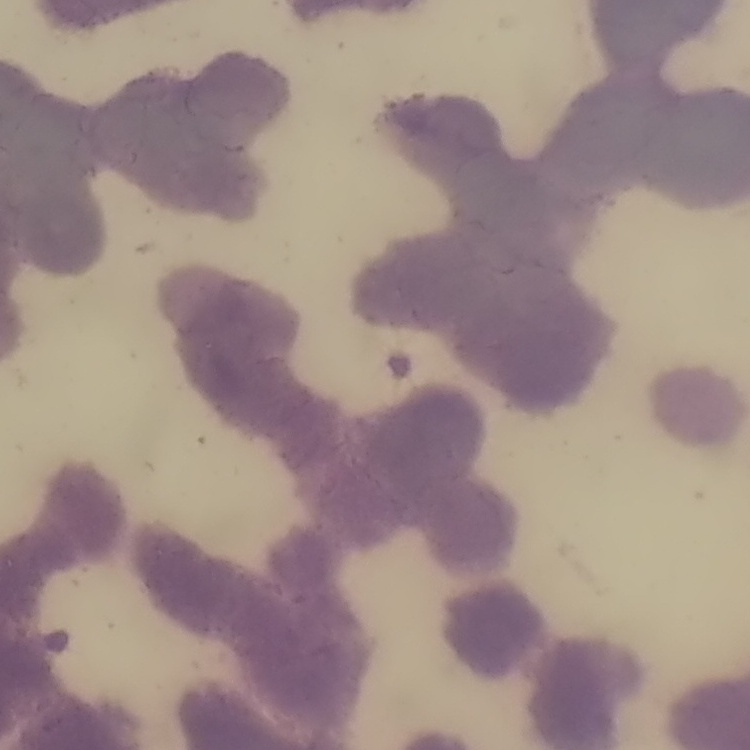

Summary:
  - Red blood cell morphology: rouleaux formation
  - Image type: square crop of a larger photomicrograph
  - Preparation: thin peripheral smear
  - Stain: Field's or Giemsa